Assess the morphology of the erythrocytes.
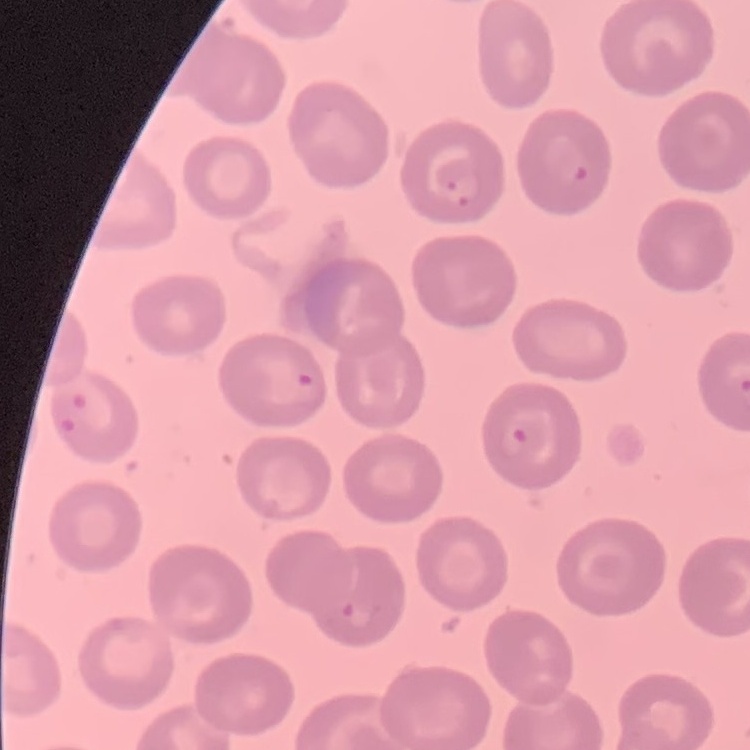

They show no rouleaux formation.

Thin peripheral smear. Stained with either Field's or Giemsa. Square crop of a larger photomicrograph.